Classify this cell by malaria status.
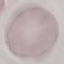
Uninfected.

Acquired by smartphone through the microscope eyepiece. Cell patch, automatically extracted from a larger field of view and resized to 64 × 64 pixels. Giemsa stain. Thin blood smear.